Assess this cell for malaria.
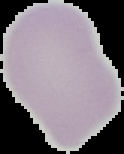

Uninfected.

Summary:
  - Preparation: thin blood smear
  - Image type: segmented cell region with the area outside set to black
  - Image size: 124×154 pixels